Look for Plasmodium parasites.
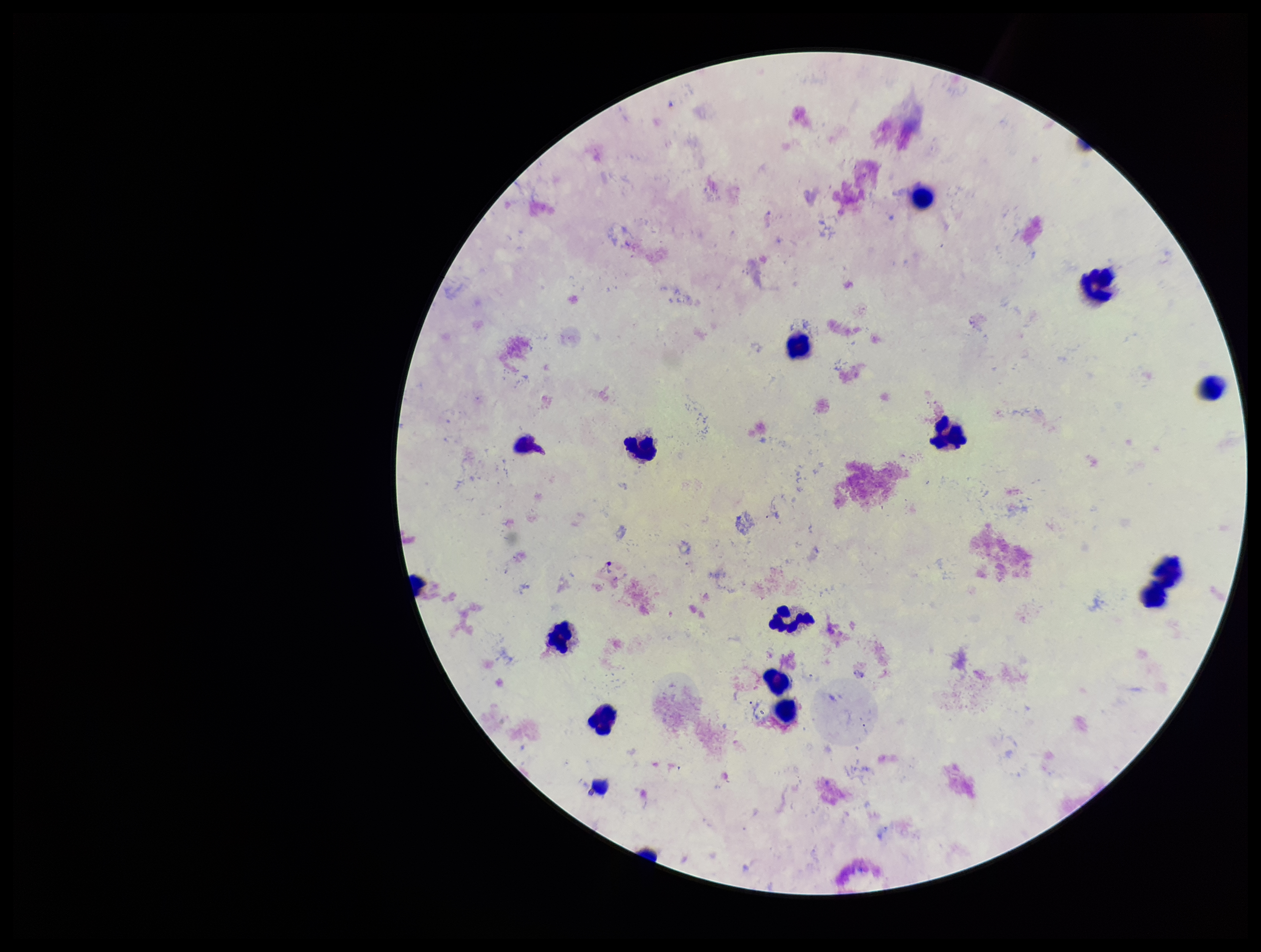

None seen.

preparation: thick smear
species_reported_for_this_patient: Plasmodium vivax
field_of_view: single
leukocyte_count: 15
capture: smartphone photograph through the microscope eyepiece
parasite_count: 0
patient_malaria_status: positive
image_size: 1261×952 pixels
stain: Giemsa